Report the malaria status of this cell.
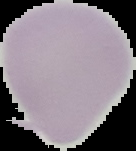
It is uninfected.

preparation = thin blood smear
image type = cell region segmented out of the field of view; surrounding area masked to black
image size = 136×151 pixels